Report the malaria status of this cell.
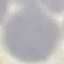
It is uninfected.

image type = cell patch, automatically extracted from a larger field of view and resized to 64 × 64 pixels
preparation = thin blood smear
stain = Giemsa
capture = smartphone camera at the microscope eyepiece